Locate every blood parasite and identify its species.
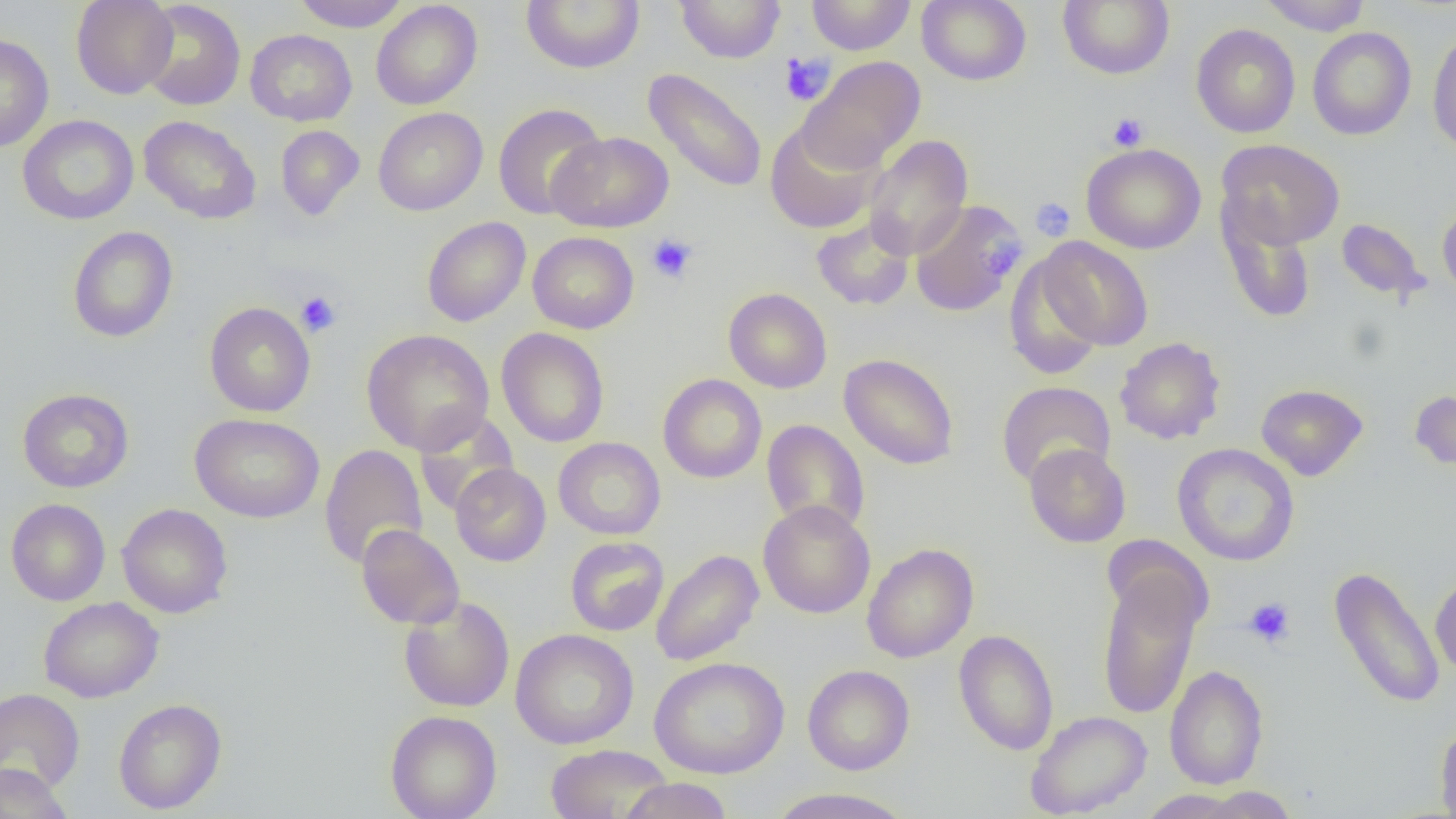
No blood parasites observed.

slide-level diagnosis = negative for blood parasites
field of view = single
image size = 1456×819 pixels
magnification = 1000x
preparation = thin blood smear
platelet locations = approximate bounding boxes as (x1, y1, x2, y2) in pixels: (779, 52, 835, 106), (1107, 112, 1149, 151), (1030, 197, 1075, 240), (647, 233, 697, 283), (985, 235, 1024, 279), (295, 291, 342, 337), (1243, 597, 1296, 647)
uninfected red blood cell locations = approximate bounding boxes as (x1, y1, x2, y2) in pixels: (71, 0, 178, 99), (292, 0, 410, 32), (521, 0, 645, 73), (675, 0, 786, 64), (806, 0, 916, 55), (917, 0, 1030, 85), (1058, 0, 1174, 80), (1260, 0, 1372, 35), (138, 1, 246, 110), (371, 1, 482, 110), (1191, 23, 1300, 138), (1427, 26, 1456, 155), (1307, 27, 1416, 140), (245, 29, 357, 126), (0, 33, 54, 152), (797, 55, 926, 174), (642, 68, 768, 194), (492, 103, 608, 220), (373, 107, 487, 216), (17, 115, 139, 225), (139, 115, 261, 224), (765, 121, 882, 234), (275, 125, 365, 220), (547, 131, 674, 232), (863, 134, 974, 261), (1216, 139, 1345, 250), (1081, 143, 1206, 254), (910, 199, 1024, 317), (1218, 199, 1317, 324), (1437, 200, 1456, 304), (422, 216, 531, 327), (810, 216, 915, 311), (1336, 219, 1430, 304), (67, 226, 178, 343), (527, 231, 639, 333), (1035, 237, 1154, 351), (1004, 254, 1108, 380), (723, 288, 832, 393), (204, 302, 316, 417), (497, 327, 610, 448), (361, 328, 494, 455), (1114, 336, 1227, 445), (839, 353, 959, 470), (657, 373, 767, 484), (996, 381, 1116, 488), (1256, 383, 1368, 481), (17, 388, 134, 493), (1409, 388, 1456, 476), (412, 409, 520, 517), (190, 412, 325, 523), (761, 419, 870, 536), (553, 437, 665, 540), (1023, 443, 1131, 547), (1173, 443, 1300, 566), (319, 444, 428, 570), (450, 463, 551, 566), (6, 498, 111, 605), (757, 500, 875, 618), (117, 503, 233, 618), (356, 524, 465, 629), (1101, 535, 1213, 637), (565, 536, 669, 636), (862, 542, 978, 663), (650, 549, 764, 667), (1095, 562, 1206, 721), (1328, 565, 1445, 711), (1430, 571, 1456, 679), (398, 595, 515, 712), (38, 597, 164, 702), (510, 628, 639, 750), (953, 629, 1059, 756), (649, 657, 789, 779), (802, 664, 915, 775), (1164, 664, 1269, 790), (0, 689, 85, 794), (113, 698, 227, 814), (386, 710, 502, 819), (1025, 710, 1152, 817), (1435, 717, 1456, 819), (545, 743, 673, 818), (0, 764, 73, 818), (617, 777, 733, 818), (1194, 787, 1299, 818), (765, 788, 915, 819), (1137, 790, 1249, 818)
modality = light microscopy